Assess this cell for malaria.
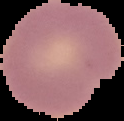
It is uninfected.

image_type: cell region segmented out of the field of view; surrounding area masked to black
image_size: 124×121 pixels
preparation: thin blood film